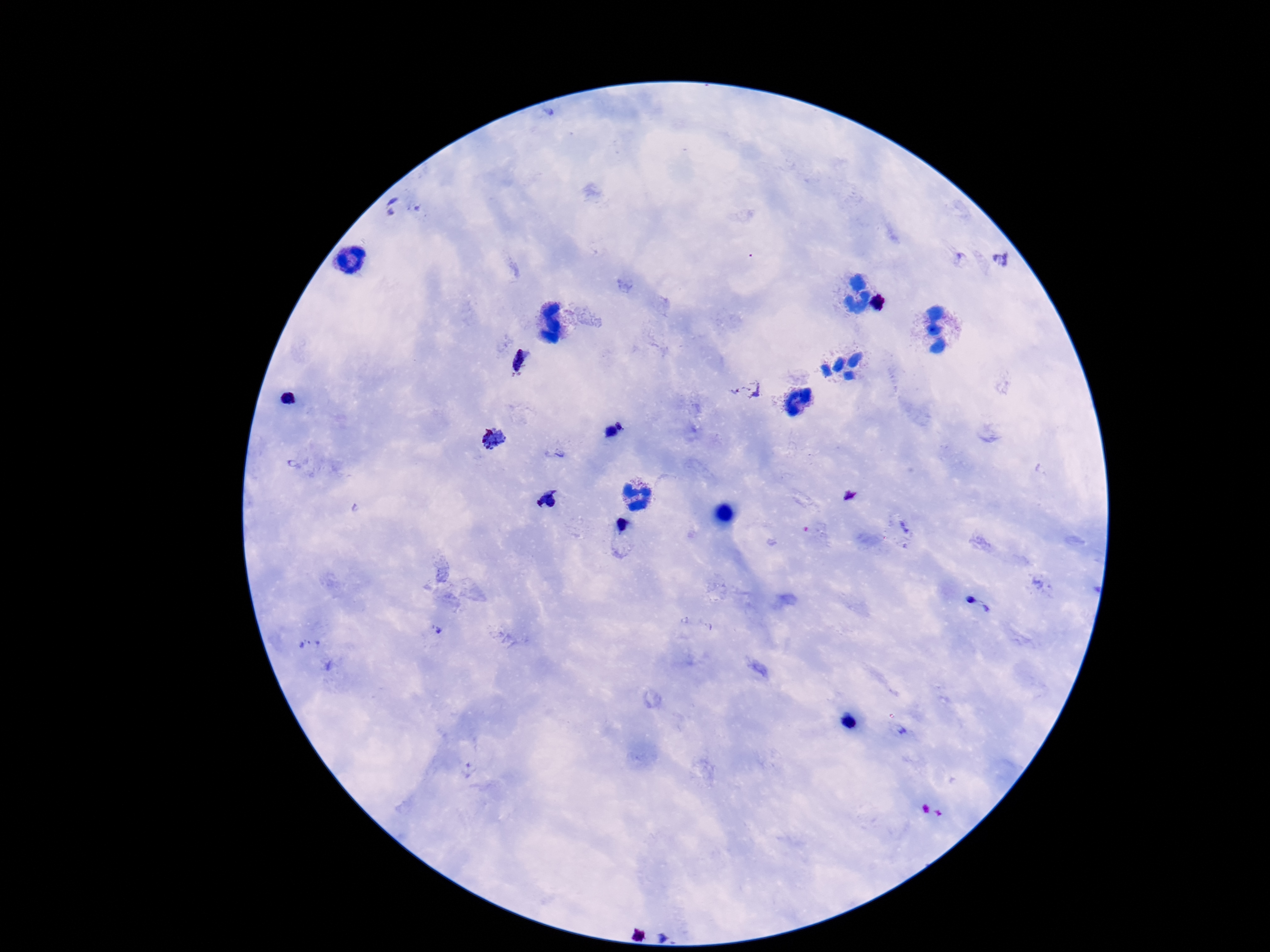

Approximate object centers, in pixels from the top-left corner.
Summary:
  - Plasmodium parasite locations: (x=395, y=206), (x=1001, y=259), (x=520, y=359), (x=748, y=391), (x=291, y=399), (x=621, y=424), (x=611, y=432), (x=494, y=439), (x=556, y=453), (x=850, y=496), (x=547, y=499), (x=623, y=527), (x=977, y=606), (x=850, y=720)
  - Stain: Giemsa
  - Patient malaria status: infected
  - Field of view: one from this slide
  - Image size: 1270×952 pixels
  - Capture: smartphone camera through the microscope eyepiece
  - Magnification: 100x
  - Preparation: thick blood smear